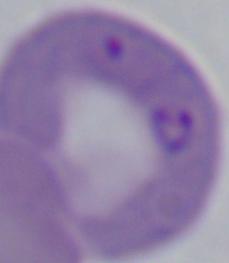
Summary:
  - Modality: photomicrograph
  - Magnification: 1000x
  - Identification: Babesia